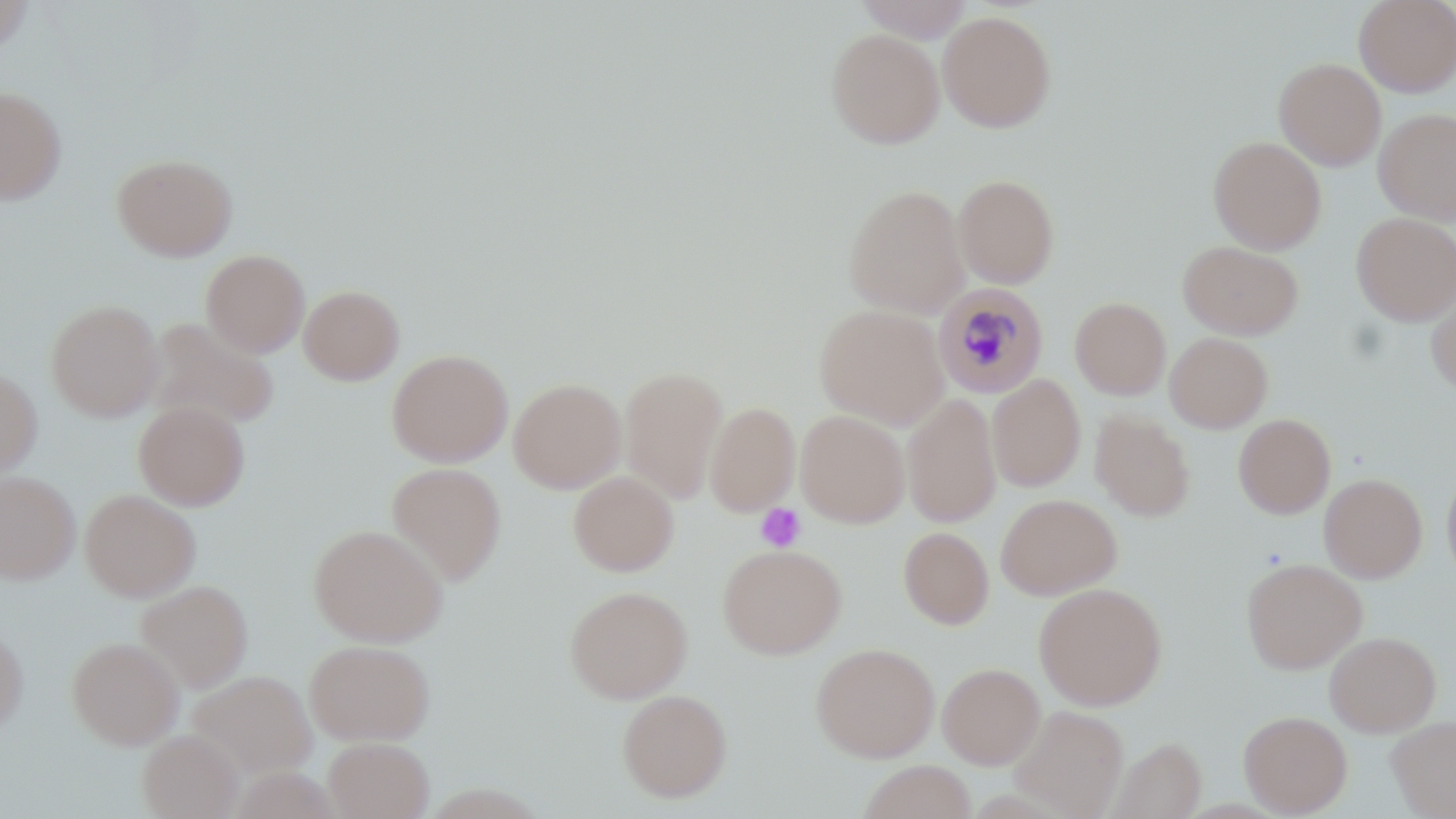
Summary:
  - Coordinate format: approximate bounding boxes as (x1, y1, x2, y2) in pixels
  - Plasmodium malariae-infected red blood cell locations: (934, 282, 1049, 398)
  - Platelet locations: (755, 503, 806, 552)
  - Uninfected red blood cell locations: (856, 0, 975, 42), (1354, 0, 1456, 97), (0, 1, 34, 57), (937, 9, 1056, 132), (825, 27, 945, 149), (1273, 58, 1386, 170), (0, 86, 67, 205), (1373, 107, 1456, 224), (1208, 136, 1326, 254), (111, 153, 238, 262), (952, 173, 1059, 289), (843, 184, 970, 317), (1351, 212, 1456, 325), (1178, 240, 1303, 339), (201, 249, 310, 357), (299, 284, 404, 385), (1426, 285, 1456, 396), (1070, 296, 1170, 400), (45, 299, 163, 422), (814, 303, 950, 429), (144, 316, 280, 430), (1164, 332, 1273, 432), (387, 349, 513, 467), (619, 366, 728, 504), (0, 369, 42, 478), (987, 374, 1086, 492), (508, 378, 626, 493), (902, 392, 1001, 528), (133, 401, 251, 510), (705, 401, 800, 516), (795, 410, 910, 527), (1090, 410, 1195, 521), (1233, 413, 1335, 518), (387, 461, 507, 586), (1442, 465, 1456, 584), (568, 470, 679, 576), (0, 471, 80, 584), (1318, 473, 1427, 583), (79, 488, 201, 602), (995, 493, 1122, 599), (308, 523, 448, 647), (898, 526, 994, 629), (717, 543, 847, 659), (1241, 557, 1367, 674), (135, 579, 253, 693), (1034, 581, 1167, 710), (564, 585, 693, 703), (0, 624, 28, 736), (1324, 631, 1441, 736), (66, 636, 184, 750), (304, 639, 435, 745), (811, 642, 939, 762), (937, 662, 1044, 768), (186, 670, 317, 779), (616, 688, 733, 802), (1009, 705, 1129, 818), (1238, 710, 1352, 817), (1387, 715, 1456, 818), (136, 728, 243, 819), (323, 737, 434, 819), (1110, 737, 1206, 818), (858, 760, 976, 818)
  - Slide-level diagnosis: Plasmodium malariae
  - Magnification: 1000x
  - Image size: 1456×819 pixels
  - Field of view: single
  - Stain: May-Grünwald-Giemsa
  - Preparation: thin blood smear
  - Modality: light microscopy